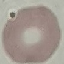

result = no malaria parasites detected
capture = smartphone through the microscope eyepiece
stain = Giemsa
image type = cell patch, automatically extracted from a larger field of view and resized to 64 × 64 pixels
preparation = thin smear